Assess this cell for malaria.
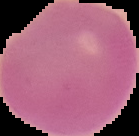

Uninfected.

Summary:
  - Image type: segmented cell region on a black background
  - Preparation: thin blood film
  - Image size: 139×136 pixels